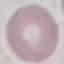

Summary:
  - Result: no malaria parasites detected
  - Image type: automatically extracted cell patch, resized to 64 × 64 pixels
  - Capture: smartphone through the microscope eyepiece
  - Preparation: thin blood smear
  - Stain: Giemsa